Name the parasite shown.
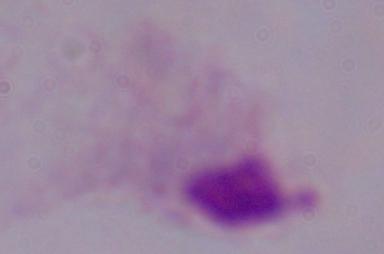

This is a trichomonad.

{
  "magnification": "1000x",
  "modality": "photomicrograph"
}